Assess the morphology of the erythrocytes.
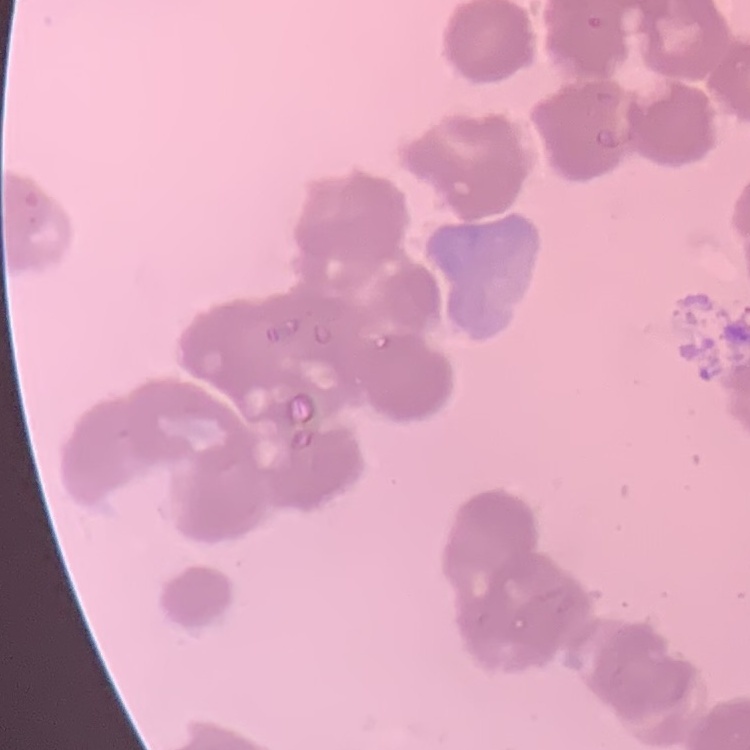
Rouleaux formation.

Summary:
  - Image type: square crop of a larger photomicrograph
  - Preparation: thin peripheral smear
  - Stain: Field's or Giemsa